Classify this cell by malaria status.
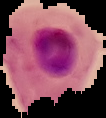

Parasitized.

image_type: segmented cell region with the area outside set to black
image_size: 106×118 pixels
preparation: thin blood smear